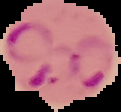

Summary:
  - Image type: segmented cell region on a black background
  - Result: malaria parasites detected
  - Image size: 121×112 pixels
  - Preparation: thin blood film